Name the parasite shown.
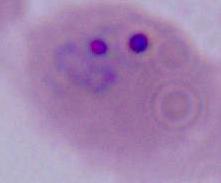

This is Plasmodium.

{
  "magnification": "400x or 1000x",
  "modality": "photomicrograph"
}